Assess for parasitized red blood cells.
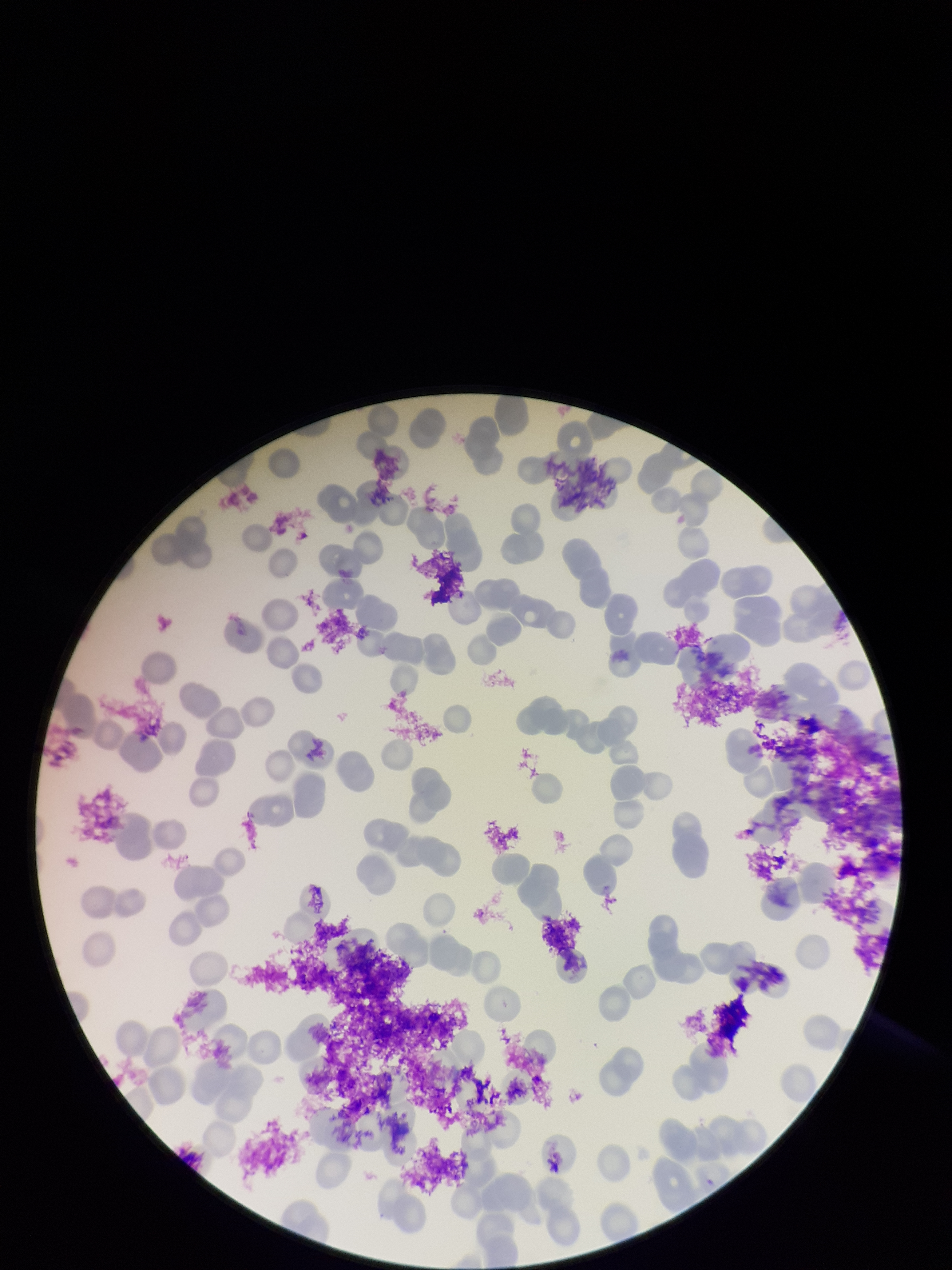
None detected.

preparation = thin blood smear
capture = smartphone photograph through the microscope eyepiece
red blood cell count = 128
parasitized red blood cell count = 0
image size = 952×1270 pixels
patient malaria status = infected
stain = Giemsa
field of view = one from this slide
species reported for this patient = Plasmodium falciparum